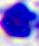
{
  "magnification": "400x",
  "identification": "leukocyte",
  "modality": "photomicrograph"
}